Report the malaria status of this cell.
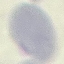

It is uninfected.

Summary:
  - Preparation: thin blood film
  - Image type: cell patch, automatically extracted from a larger field of view and resized to 64 × 64 pixels
  - Stain: Giemsa
  - Capture: smartphone camera at the microscope eyepiece